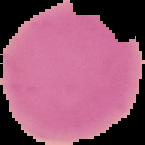

Image is 145×145 pixels. The area outside the segmented cell region is set to black. From a thin blood smear. Result: no malaria parasites detected.